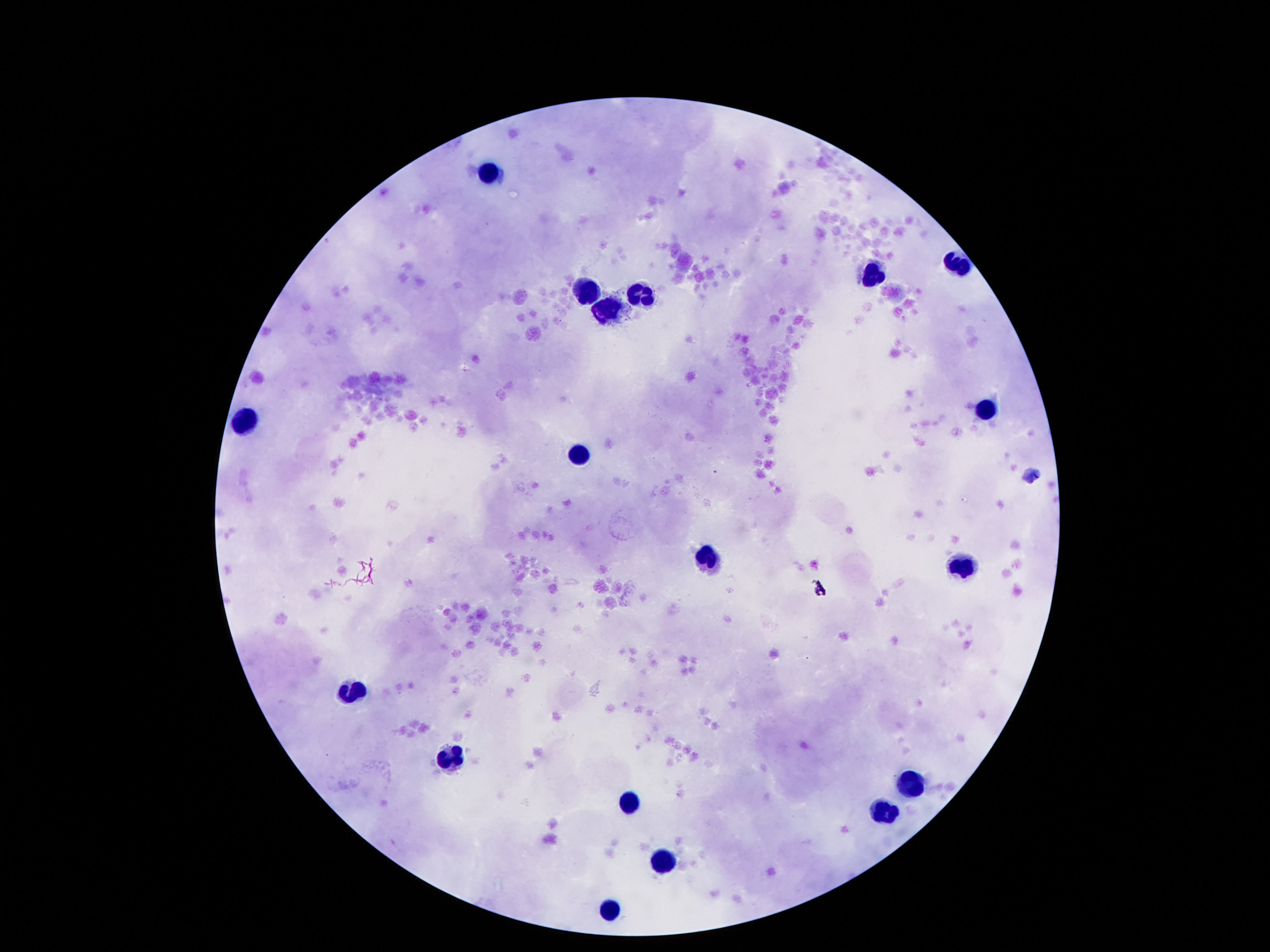

{
  "stain": "Giemsa",
  "capture": "smartphone camera through the microscope eyepiece",
  "patient_malaria_status": "uninfected",
  "image_size": "1270×952 pixels",
  "magnification": "100x",
  "leukocyte_locations": "approximate centers as {x, y} in pixels: {487, 174}, {960, 264}, {874, 273}, {586, 294}, {639, 294}, {607, 312}, {982, 411}, {243, 421}, {577, 452}, {708, 559}, {962, 570}, {355, 689}, {450, 762}, {909, 786}, {631, 801}, {883, 816}, {663, 861}, {607, 910}",
  "field_of_view": "single",
  "preparation": "thick blood film"
}